Report the malaria status of this cell.
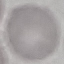
It is uninfected.

Summary:
  - Capture: smartphone camera at the microscope eyepiece
  - Stain: Giemsa
  - Preparation: thin blood smear
  - Image type: automatically extracted cell patch, resized to 64 × 64 pixels